Assess this cell for malaria.
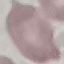

Uninfected.

{
  "image_type": "automatically extracted cell patch, resized to 64 × 64 pixels",
  "capture": "smartphone camera at the microscope eyepiece",
  "preparation": "thin smear",
  "stain": "Giemsa"
}